Assess the morphology of the red blood cells.
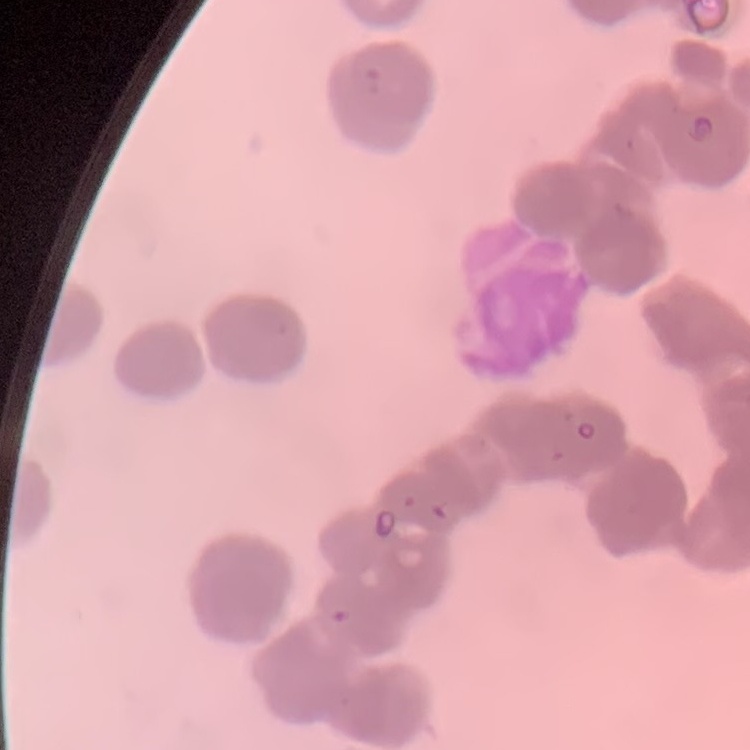
Rouleaux formation.

stain: Field's or Giemsa
image_type: one tile cut from a larger photomicrograph
preparation: thin blood film